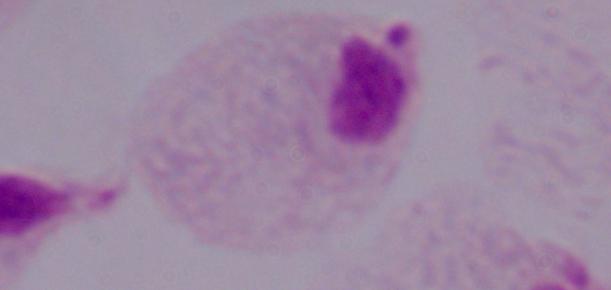

Photomicrograph. 1000x magnification. A trichomonad is seen.